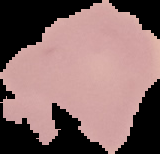
malaria status = uninfected
image type = cell region segmented out of the field of view; surrounding area masked to black
image size = 160×154 pixels
preparation = thin blood film